Comment on the morphology of the erythrocytes.
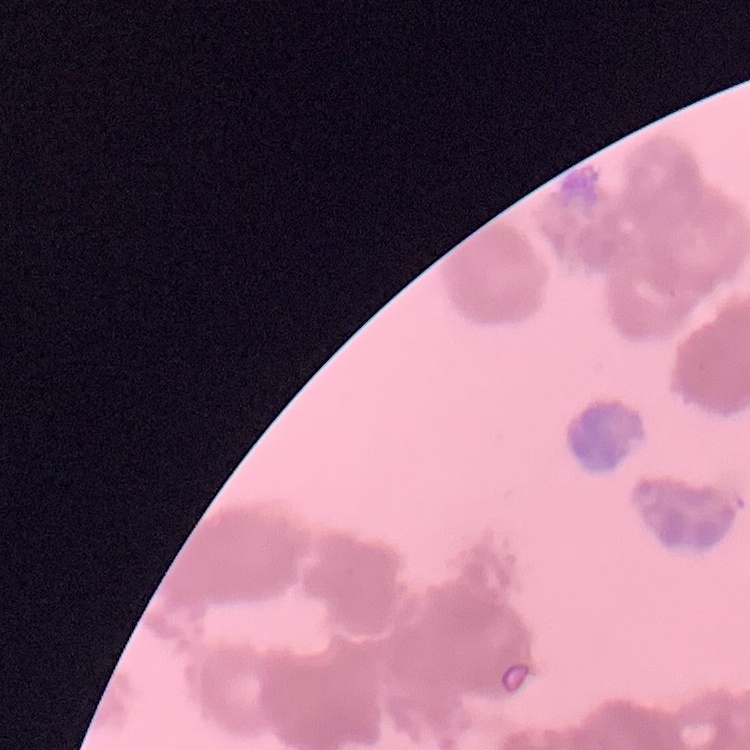
Rouleaux formation.

image type = one tile cut from a larger photomicrograph
preparation = thin peripheral smear
stain = Field's or Giemsa